Locate and identify every blood parasite.
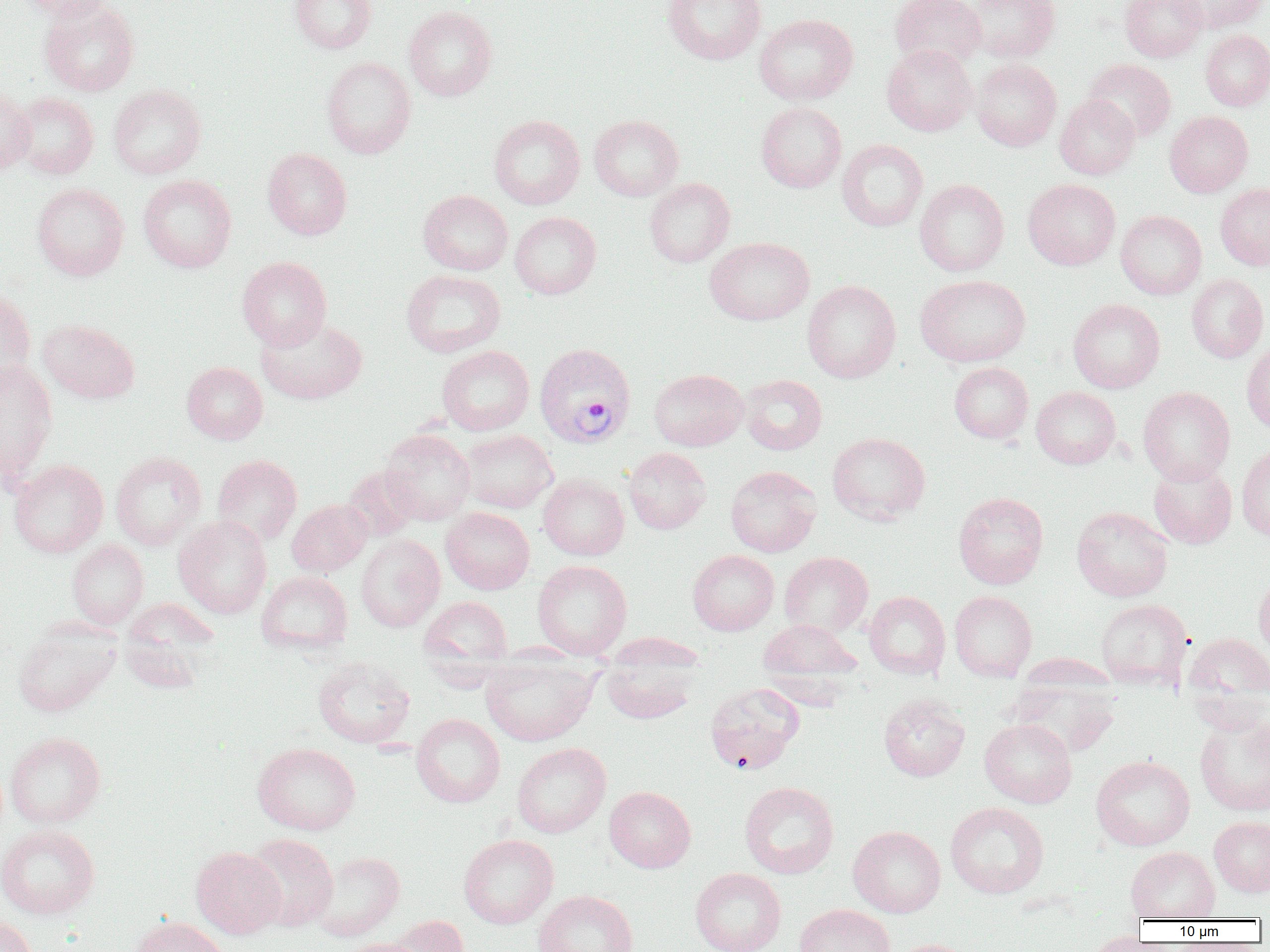
Approximate bounding boxes as (x1,y1)-(x2,y2) corner pairs in pixels.
Plasmodium vivax-infected red blood cells: (534,342)-(635,447).
No Plasmodium falciparum, Plasmodium ovale, Plasmodium malariae, Babesia divergens, or Trypanosoma brucei observed.

Uninfected red blood cell locations: (15,0)-(116,21), (38,0)-(139,96), (289,0)-(376,54), (662,0)-(766,64), (890,0)-(986,71), (967,0)-(1060,62), (1120,0)-(1207,62), (1173,0)-(1267,33), (403,6)-(497,101), (754,14)-(857,105), (1200,29)-(1270,111), (881,44)-(977,136), (321,56)-(416,159), (971,58)-(1062,151), (1083,59)-(1176,142), (108,84)-(206,179), (0,88)-(35,174), (12,93)-(99,179), (1055,95)-(1140,180), (756,102)-(847,193), (1164,111)-(1253,197), (488,115)-(585,209), (589,115)-(683,201), (837,139)-(928,231), (263,148)-(352,239), (138,174)-(236,273), (644,178)-(735,267), (914,179)-(1009,277), (1023,179)-(1120,270), (32,183)-(129,281), (1215,184)-(1270,270), (418,190)-(513,276), (1116,210)-(1206,300), (509,211)-(601,299), (704,237)-(814,325), (236,256)-(332,350), (401,269)-(505,357), (1186,273)-(1268,363), (915,274)-(1031,367), (802,280)-(901,383), (0,288)-(36,391), (1068,299)-(1165,393), (256,316)-(367,405), (38,319)-(140,404), (1241,339)-(1270,434), (437,345)-(534,435), (0,361)-(58,483), (181,362)-(268,444), (949,362)-(1033,443), (648,368)-(748,451), (739,374)-(827,455), (1031,386)-(1121,468), (1138,386)-(1235,485), (380,429)-(475,525), (460,429)-(557,513), (827,432)-(930,525), (1236,444)-(1270,541), (623,447)-(711,534), (110,451)-(207,549), (212,454)-(302,545), (8,459)-(108,557), (1149,461)-(1237,548), (725,465)-(822,557), (343,466)-(421,541), (538,473)-(629,560), (953,491)-(1049,589), (287,499)-(372,577), (1072,506)-(1173,602), (441,507)-(535,594), (173,515)-(271,619), (355,534)-(445,632), (67,540)-(148,628), (687,549)-(779,635), (779,551)-(873,638), (532,559)-(632,659), (256,571)-(353,654), (1253,571)-(1270,662), (949,590)-(1037,681), (864,591)-(950,679), (419,596)-(513,673), (121,597)-(219,682), (1096,598)-(1192,690), (758,619)-(862,692), (13,621)-(120,717), (1183,631)-(1270,715), (604,632)-(706,673), (599,655)-(702,724), (312,656)-(415,748), (479,656)-(598,746), (1008,670)-(1121,758), (704,682)-(805,774), (879,693)-(970,781), (1194,712)-(1270,817), (411,713)-(505,807), (979,717)-(1077,808), (5,732)-(106,828), (252,742)-(361,835), (512,742)-(611,838), (1091,755)-(1195,851), (740,781)-(839,878), (604,786)-(695,873), (945,801)-(1049,898), (1209,816)-(1270,897), (0,824)-(100,919), (848,825)-(945,917), (244,833)-(338,931), (458,834)-(559,929), (1125,846)-(1219,921), (190,847)-(286,938), (309,851)-(405,941), (690,868)-(786,952), (534,890)-(637,952), (795,904)-(896,952), (0,916)-(37,952), (128,916)-(230,952), (387,916)-(470,952), (1080,932)-(1160,952), (337,937)-(426,952), (886,939)-(978,952). Slide-level diagnosis: Plasmodium vivax. Optical microscopy. Thin blood smear. Captured at 1000x magnification. One field of a larger specimen. Image is 1270×952 pixels.